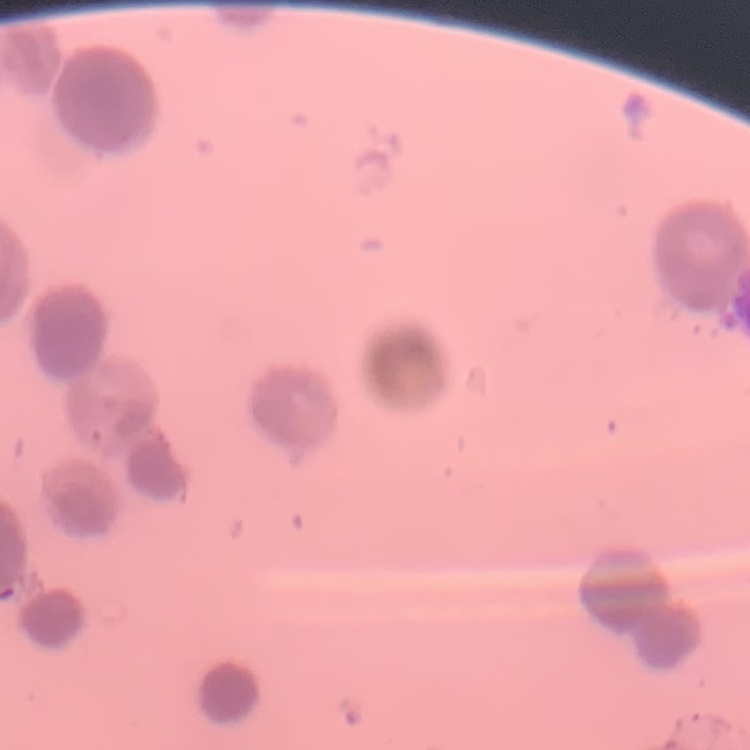

erythrocyte morphology = rouleaux formation
stain = Field's or Giemsa
preparation = thin peripheral smear
image type = square crop of a larger photomicrograph